Classify this cell by malaria status.
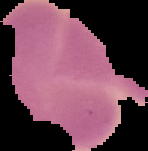
It is uninfected.

Summary:
  - Preparation: thin blood film
  - Image type: segmented cell region on a black background
  - Image size: 148×151 pixels